Comment on the morphology of the red blood cells.
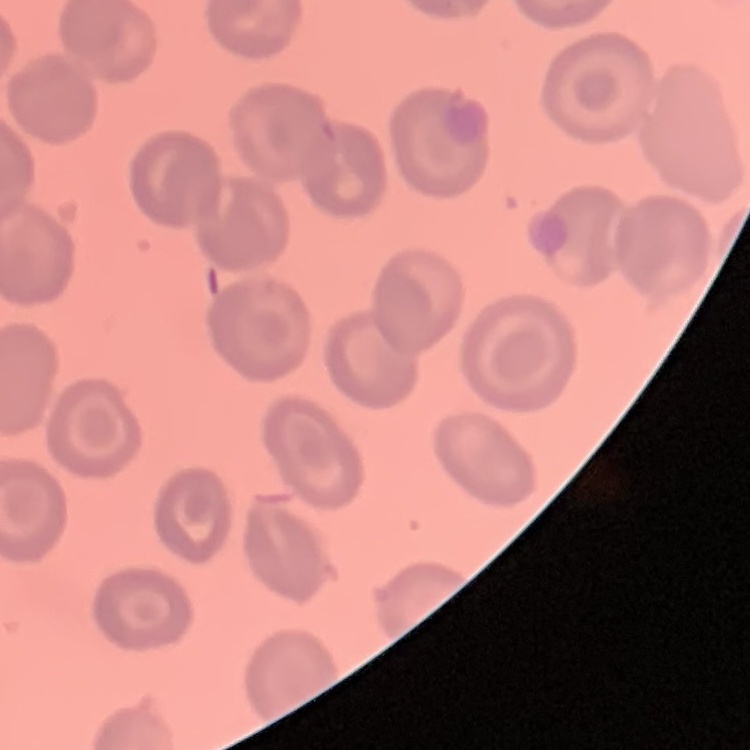
No rouleaux formation.

Summary:
  - Image type: one tile cut from a larger photomicrograph
  - Stain: Field's or Giemsa
  - Preparation: thin blood film